Name the cell type shown.
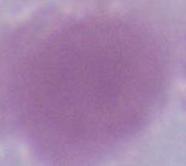
An erythrocyte.

Captured at 1000x magnification. Micrograph.